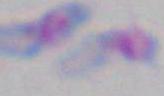
Summary:
  - Modality: micrograph
  - Magnification: 1000x
  - Identification: Toxoplasma gondii